Assess for malaria.
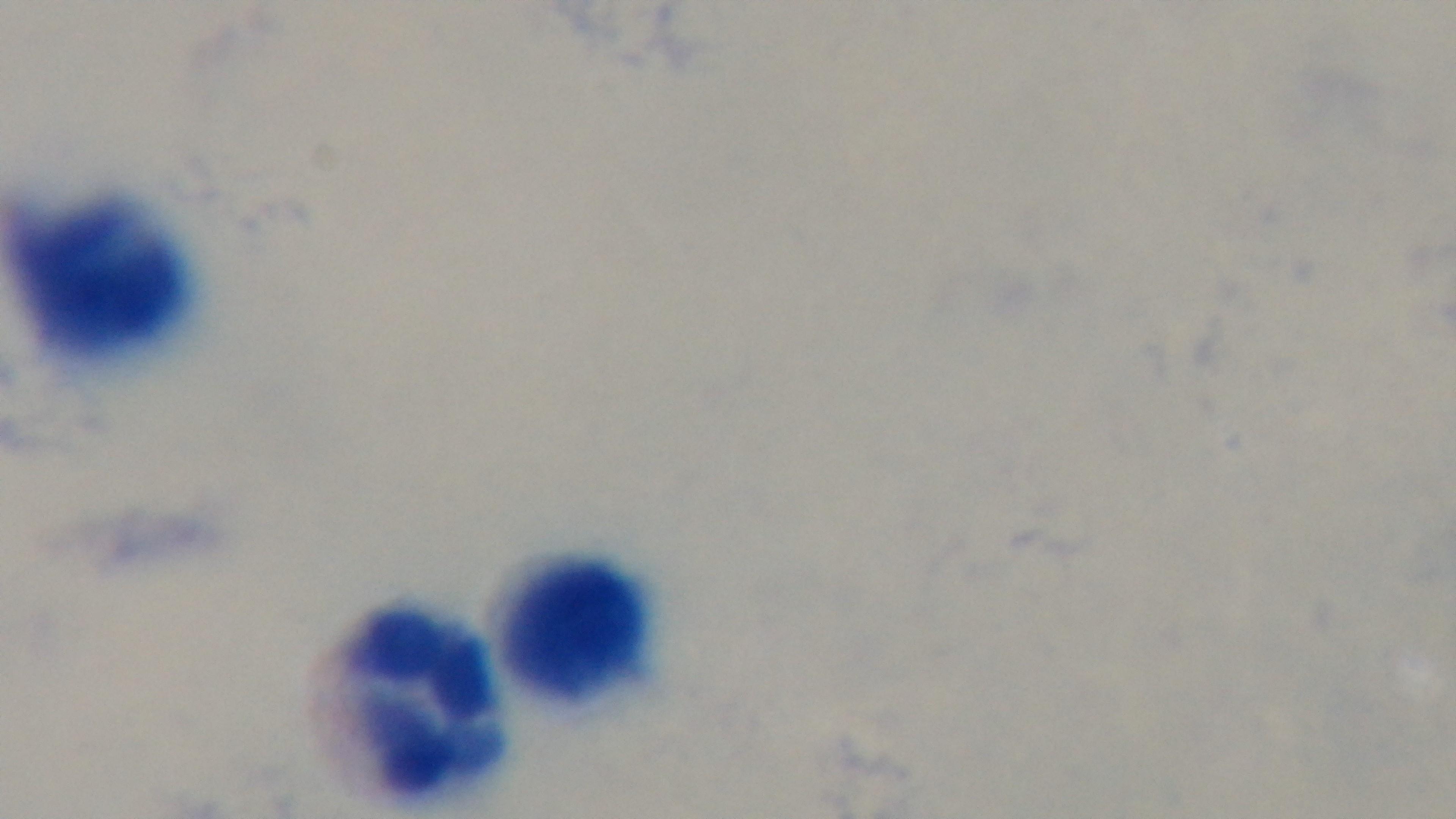

Negative.

field of view = single
modality = light microscopy
objective = 100x oil immersion
stain = Giemsa
capture = mounted 4K digital camera
preparation = thick blood film